Outline each blood parasite and name the species.
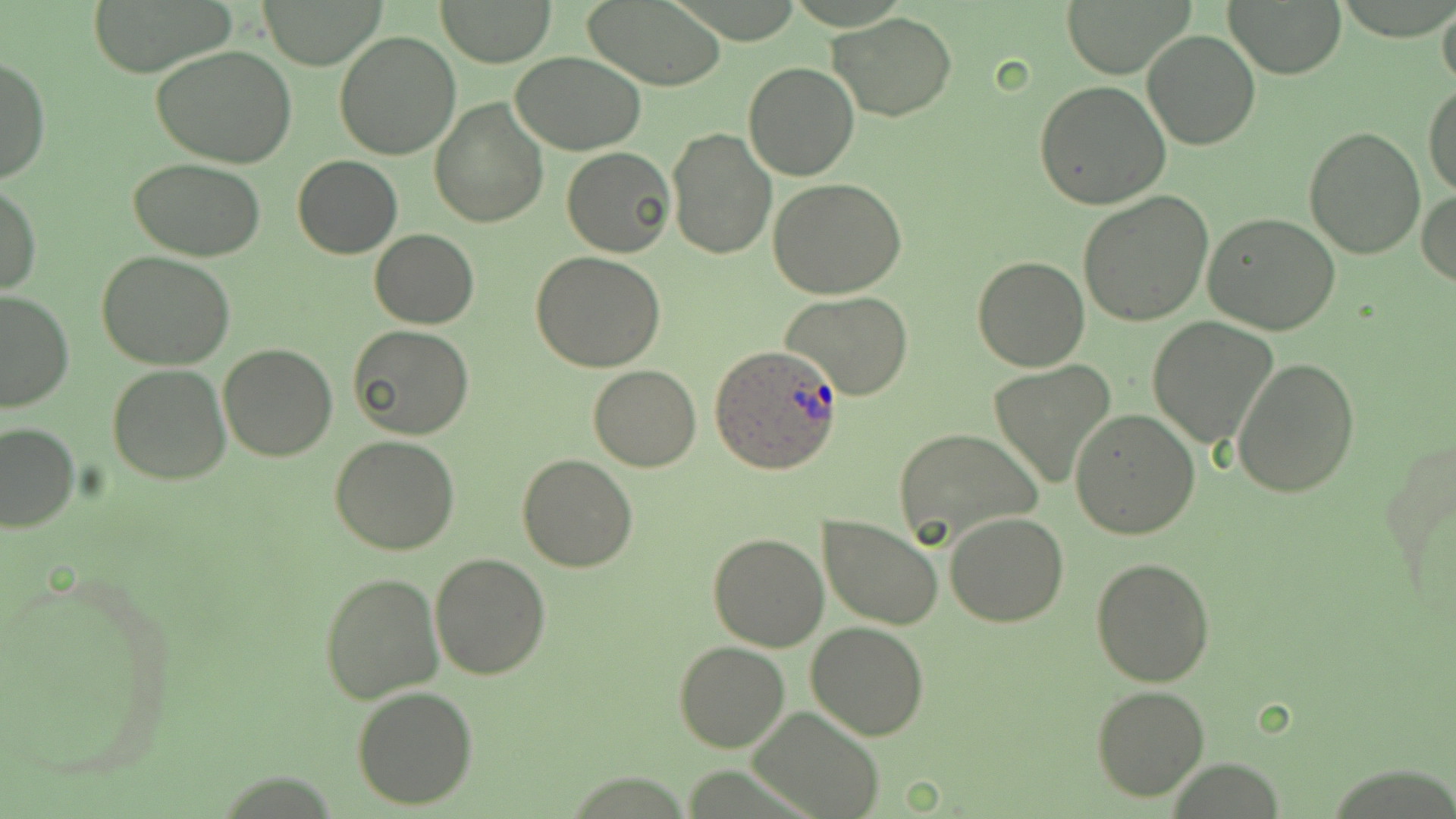
Approximate bounding boxes as [x1, y1, x2, y2] in pixels.
Plasmodium ovale-infected red blood cells: [710, 344, 843, 472].
No Plasmodium falciparum, Plasmodium malariae, Plasmodium vivax, Babesia divergens, or Trypanosoma brucei observed.

slide-level diagnosis = Plasmodium ovale
preparation = thin blood film
field of view = one of a larger specimen
magnification = 1000x
stain = May-Grünwald-Giemsa
modality = light microscopy
uninfected red blood cell locations = approximate bounding boxes as [x1, y1, x2, y2] in pixels: [85, 0, 233, 75], [435, 0, 557, 67], [578, 0, 729, 89], [262, 1, 381, 67], [1059, 1, 1191, 78], [1226, 1, 1345, 78], [1437, 1, 1456, 96], [830, 12, 957, 121], [1141, 30, 1261, 150], [332, 31, 460, 161], [153, 46, 300, 169], [511, 52, 646, 155], [1, 56, 51, 187], [742, 61, 860, 182], [1034, 80, 1170, 208], [1424, 80, 1456, 199], [429, 96, 548, 228], [1304, 126, 1425, 259], [665, 127, 778, 262], [561, 146, 675, 258], [293, 155, 401, 259], [129, 158, 265, 261], [767, 179, 908, 299], [1, 184, 40, 296], [1079, 189, 1215, 325], [1417, 189, 1456, 291], [1202, 213, 1343, 335], [370, 228, 478, 330], [97, 251, 236, 370], [532, 253, 664, 371], [972, 254, 1090, 372], [0, 290, 74, 413], [780, 292, 914, 402], [1147, 317, 1277, 448], [348, 325, 474, 440], [218, 344, 339, 461], [1232, 357, 1360, 498], [106, 362, 232, 484], [987, 362, 1115, 488], [588, 364, 702, 472], [1071, 409, 1200, 538], [0, 422, 80, 532], [892, 427, 1042, 549], [1379, 433, 1454, 609], [329, 436, 460, 555], [516, 453, 637, 571], [946, 511, 1069, 626], [820, 514, 943, 629], [708, 533, 829, 652], [429, 553, 550, 680], [1090, 557, 1216, 687], [0, 565, 178, 789], [318, 570, 443, 704], [805, 619, 930, 739], [674, 641, 791, 752], [352, 685, 477, 810], [1091, 685, 1211, 802], [750, 706, 884, 819]
image size = 1456×819 pixels